Locate every uninfected red blood cell.
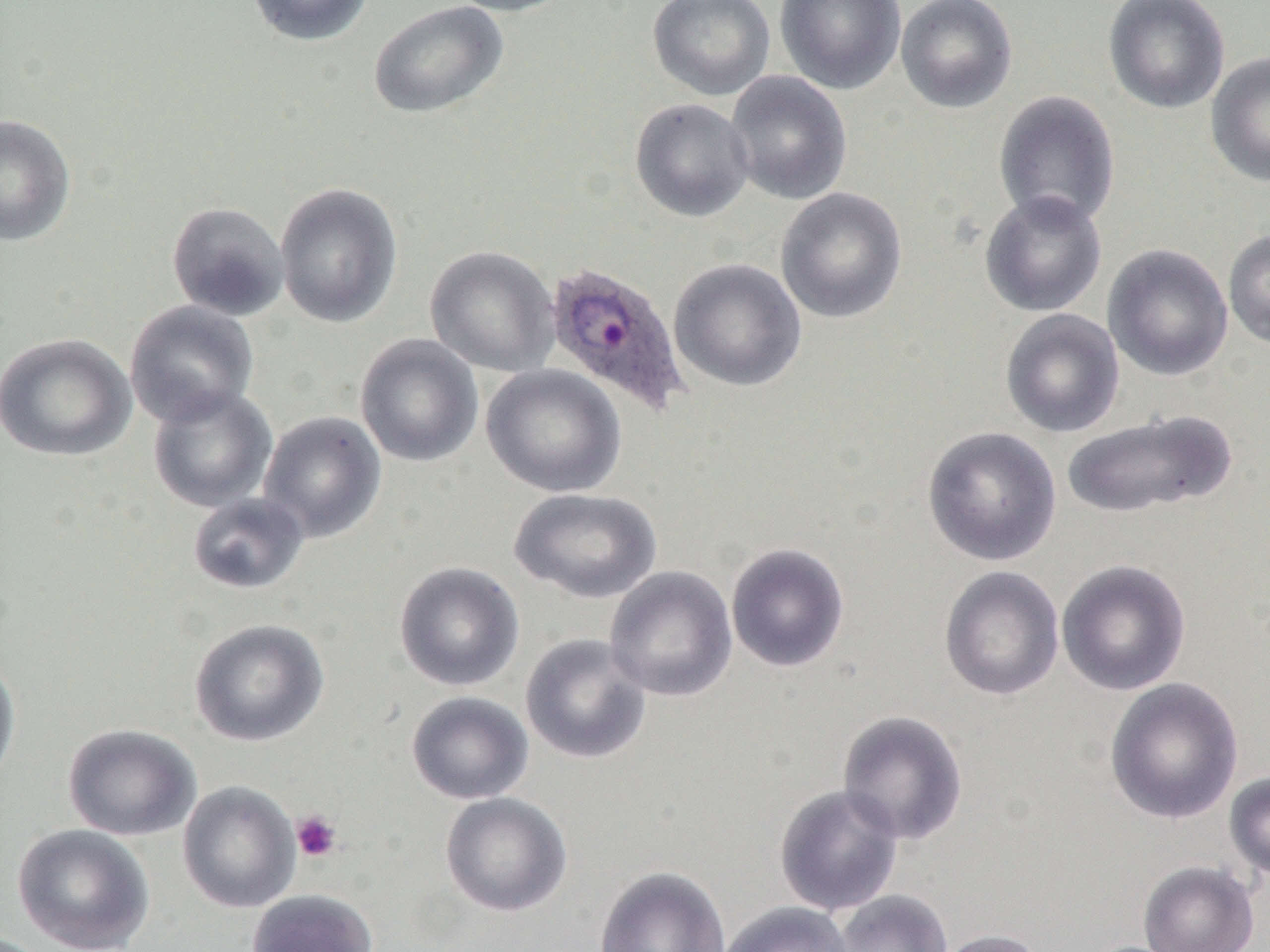
Approximate bounding boxes as (x1, y1, x2, y2) in pixels.
Uninfected red blood cells: (245, 0, 375, 47), (440, 0, 576, 17), (647, 0, 776, 101), (774, 0, 907, 95), (896, 0, 1018, 113), (1103, 0, 1230, 114), (368, 1, 509, 119), (1205, 51, 1270, 187), (725, 70, 853, 205), (993, 90, 1121, 230), (630, 98, 755, 222), (0, 114, 77, 246), (275, 182, 404, 329), (775, 187, 908, 324), (978, 190, 1108, 317), (166, 201, 290, 321), (1223, 228, 1270, 350), (1103, 243, 1233, 381), (425, 245, 559, 377), (668, 258, 807, 392), (125, 300, 259, 427), (1000, 309, 1124, 438), (1, 333, 136, 461), (355, 334, 483, 467), (481, 364, 627, 498), (148, 385, 277, 512), (1060, 409, 1236, 520), (258, 410, 387, 543), (921, 426, 1062, 566), (510, 488, 662, 603), (187, 492, 309, 595), (725, 542, 850, 672), (1056, 559, 1191, 696), (394, 561, 525, 692), (938, 565, 1065, 701), (604, 566, 738, 702), (189, 618, 329, 747), (520, 633, 652, 764), (0, 655, 21, 790), (1105, 677, 1243, 824), (406, 691, 533, 805), (836, 709, 969, 845), (63, 723, 201, 841), (1224, 771, 1270, 880), (177, 780, 302, 913), (773, 783, 904, 916), (440, 792, 572, 917), (11, 823, 155, 952), (1138, 860, 1259, 952), (594, 864, 730, 952), (247, 889, 379, 952), (832, 889, 952, 952), (718, 901, 854, 952), (930, 928, 1047, 952).

Summary:
  - Plasmodium ovale-infected red blood cell locations: (544, 262, 690, 415)
  - Platelet locations: (291, 810, 342, 862)
  - Slide-level diagnosis: Plasmodium ovale
  - Image size: 1270×952 pixels
  - Preparation: thin blood film
  - Modality: optical microscopy
  - Field of view: one of a larger specimen
  - Magnification: 1000x